Locate every uninfected red blood cell.
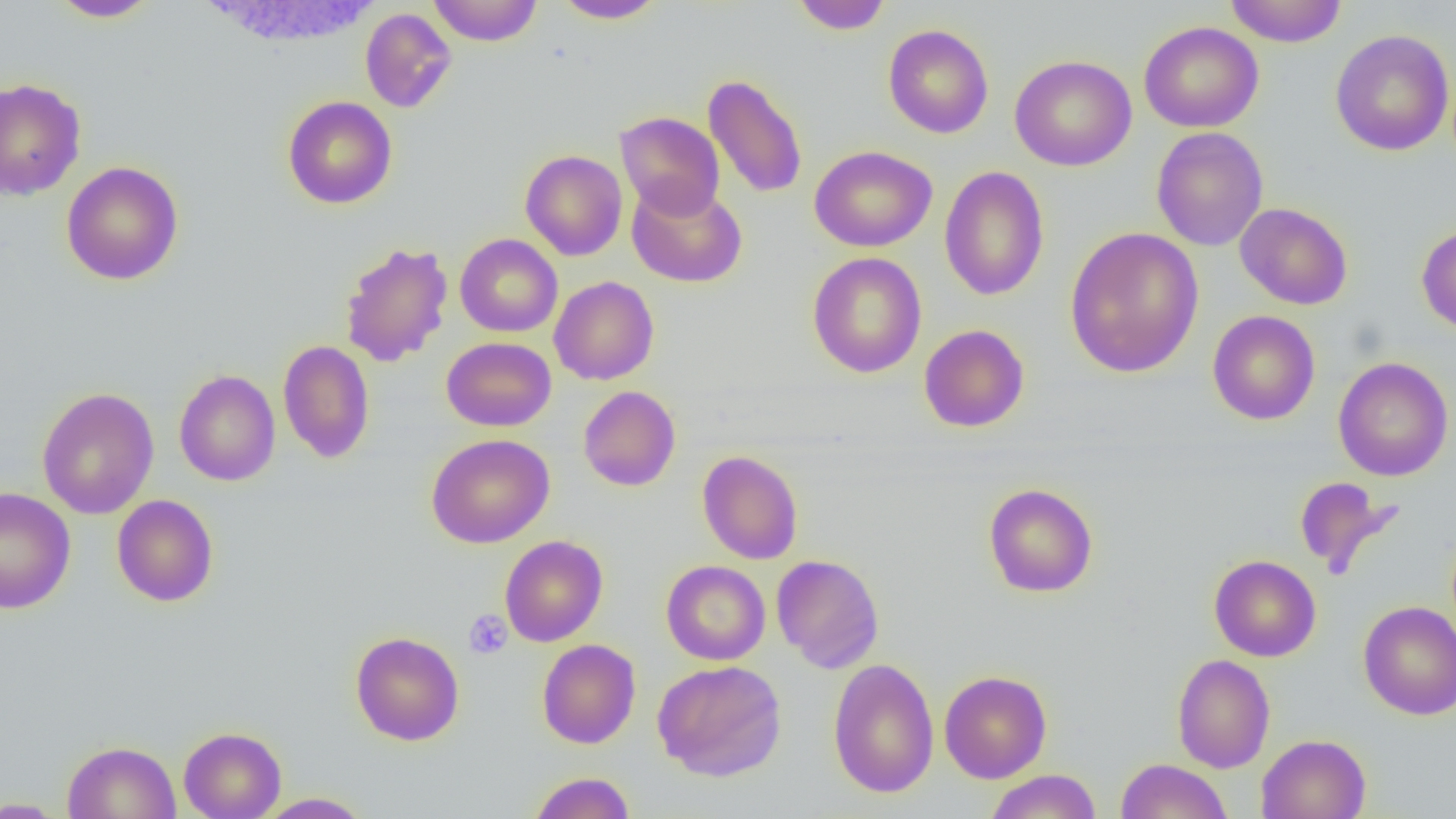
Approximate bounding boxes as [x1, y1, x2, y2] in pixels.
Uninfected red blood cells: [50, 0, 161, 22], [428, 0, 542, 46], [551, 0, 667, 24], [790, 0, 893, 34], [1224, 0, 1347, 47], [359, 8, 457, 113], [1139, 21, 1264, 133], [883, 24, 994, 138], [1330, 29, 1455, 156], [1009, 55, 1137, 171], [703, 73, 807, 199], [0, 78, 86, 201], [283, 96, 397, 209], [615, 111, 725, 220], [1151, 126, 1268, 251], [809, 145, 937, 252], [520, 149, 628, 261], [61, 161, 184, 285], [939, 166, 1050, 301], [626, 180, 747, 288], [1235, 202, 1353, 310], [1416, 224, 1456, 336], [1065, 226, 1204, 379], [455, 234, 563, 337], [339, 241, 454, 368], [807, 252, 927, 378], [550, 276, 659, 385], [1207, 310, 1320, 425], [918, 324, 1030, 432], [442, 337, 556, 431], [278, 340, 375, 463], [1333, 357, 1454, 481], [174, 369, 281, 486], [578, 385, 681, 491], [36, 387, 159, 519], [426, 433, 555, 549], [696, 450, 804, 564], [1293, 476, 1402, 580], [983, 483, 1098, 598], [0, 487, 76, 613], [112, 495, 219, 607], [499, 535, 608, 647], [771, 554, 885, 673], [1209, 554, 1321, 661], [661, 560, 771, 665], [1358, 600, 1456, 720], [350, 631, 465, 746], [537, 639, 641, 749], [1172, 653, 1275, 773], [827, 657, 940, 798], [652, 659, 787, 781], [939, 670, 1052, 784], [178, 726, 286, 819], [1256, 733, 1372, 819], [62, 740, 181, 819], [1115, 758, 1232, 819], [984, 769, 1102, 819], [527, 772, 636, 819], [254, 792, 375, 818], [0, 797, 69, 818].

slide_level_diagnosis: negative for blood parasites
image_size: 1456×819 pixels
preparation: thin blood film
modality: light microscopy
platelet_locations: 'approximate bounding boxes as [x1, y1, x2, y2] in pixels: [463, 610, 512, 660]'
field_of_view: one of a larger specimen
magnification: 1000x